Describe the morphology of the red blood cells.
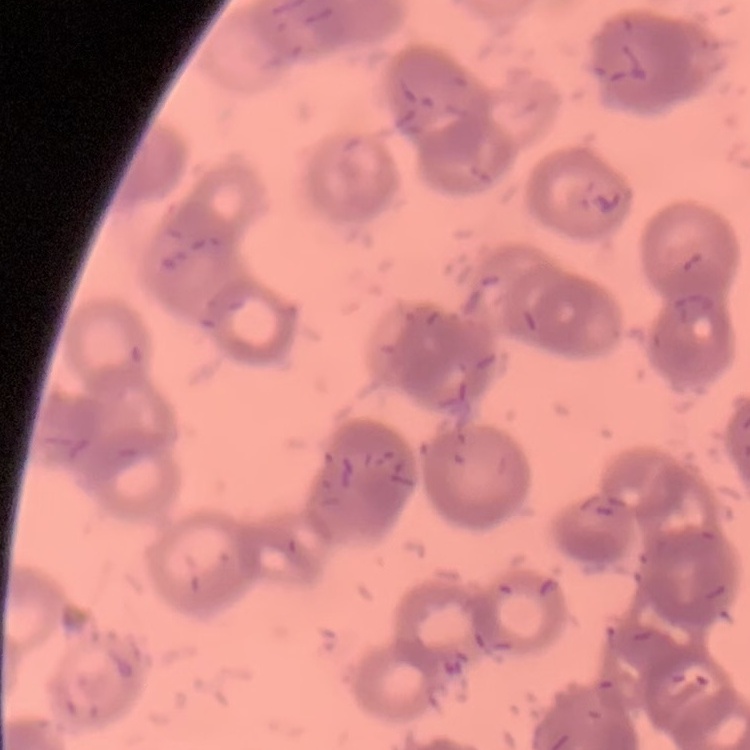

Rouleaux formation.

Stained with either Field's or Giemsa. Square crop of a larger photomicrograph. Thin blood film.